Classify this cell by malaria status.
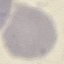
It is uninfected.

Summary:
  - Preparation: thin blood film
  - Stain: Giemsa
  - Image type: automatically extracted cell patch, resized to 64 × 64 pixels
  - Capture: smartphone through the microscope eyepiece